Locate and identify every blood parasite.
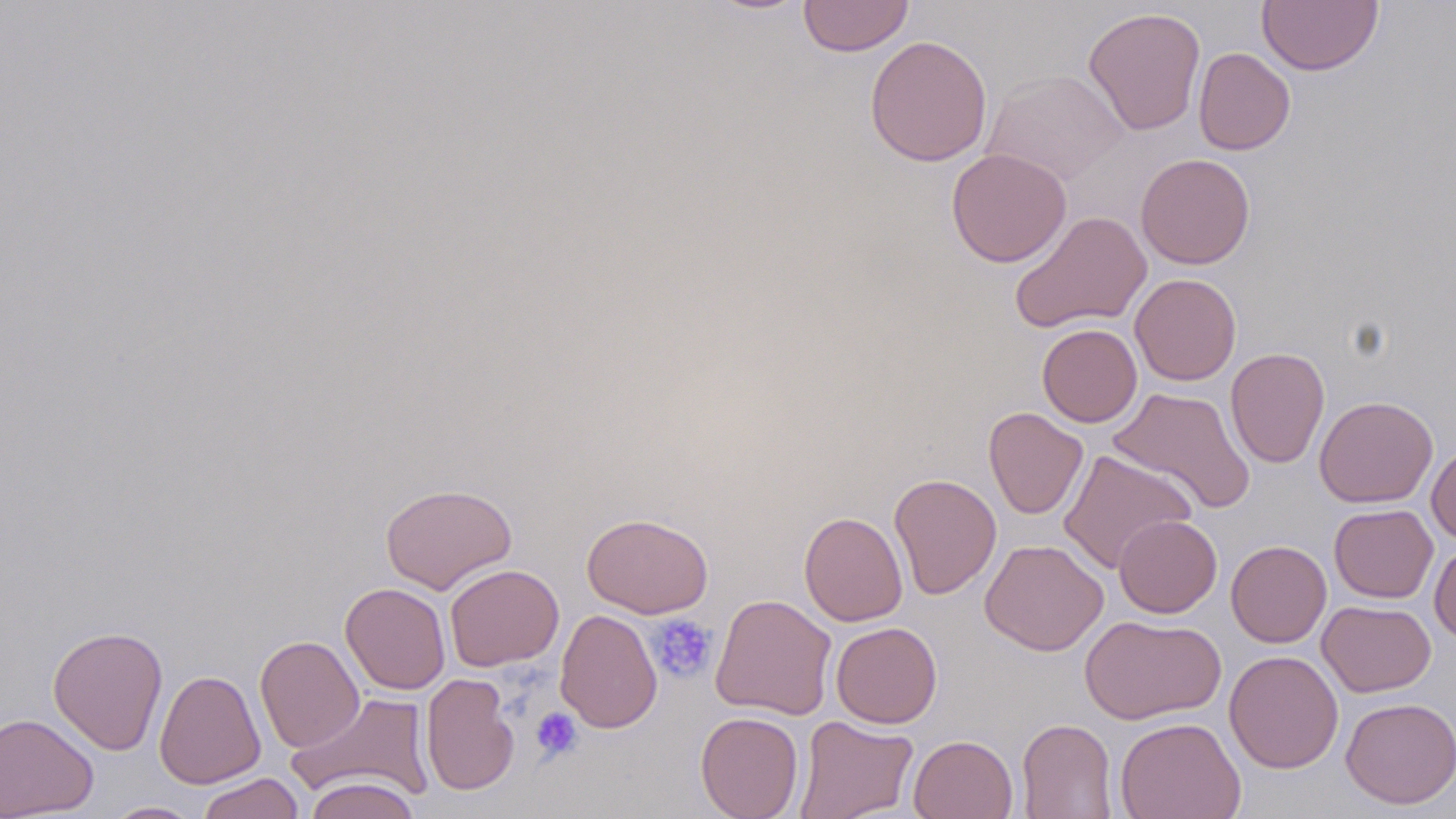

No blood parasites seen.

Summary:
  - Coordinate format: approximate bounding boxes as (x1,y1)-(x2,y2) corner pairs in pixels
  - Uninfected red blood cell locations: (798,0)-(913,57), (1256,0)-(1383,76), (1082,6)-(1206,136), (864,35)-(993,167), (1193,47)-(1296,155), (981,69)-(1127,186), (946,148)-(1072,267), (1135,153)-(1256,269), (1009,211)-(1152,333), (1129,273)-(1241,386), (1037,324)-(1142,427), (1225,347)-(1330,468), (1108,386)-(1255,514), (1314,395)-(1438,508), (984,407)-(1088,519), (1426,444)-(1456,543), (1058,450)-(1197,573), (889,473)-(1002,600), (379,483)-(518,593), (1328,504)-(1438,603), (799,511)-(908,626), (581,513)-(714,618), (1114,514)-(1222,618), (980,538)-(1108,656), (1226,540)-(1331,648), (1429,540)-(1456,644), (444,564)-(564,671), (341,582)-(450,694), (710,593)-(837,720), (1317,600)-(1436,697), (554,609)-(662,733), (1079,614)-(1226,725), (831,622)-(942,728), (47,625)-(168,755), (255,635)-(364,753), (1224,650)-(1343,773), (154,669)-(266,789), (421,673)-(520,795), (288,692)-(434,803), (1340,696)-(1456,809), (695,711)-(804,819), (0,712)-(98,817), (794,715)-(918,818), (1115,716)-(1245,819), (1017,718)-(1117,818), (909,734)-(1018,819), (196,772)-(305,819), (303,776)-(421,819), (103,801)-(204,818)
  - Platelet locations: (647,614)-(718,683), (530,707)-(583,762)
  - Slide-level diagnosis: negative for blood parasites
  - Stain: May-Grünwald-Giemsa
  - Field of view: single
  - Preparation: thin blood smear
  - Image size: 1456×819 pixels
  - Modality: light microscopy
  - Magnification: 1000x